Locate every Plasmodium parasite.
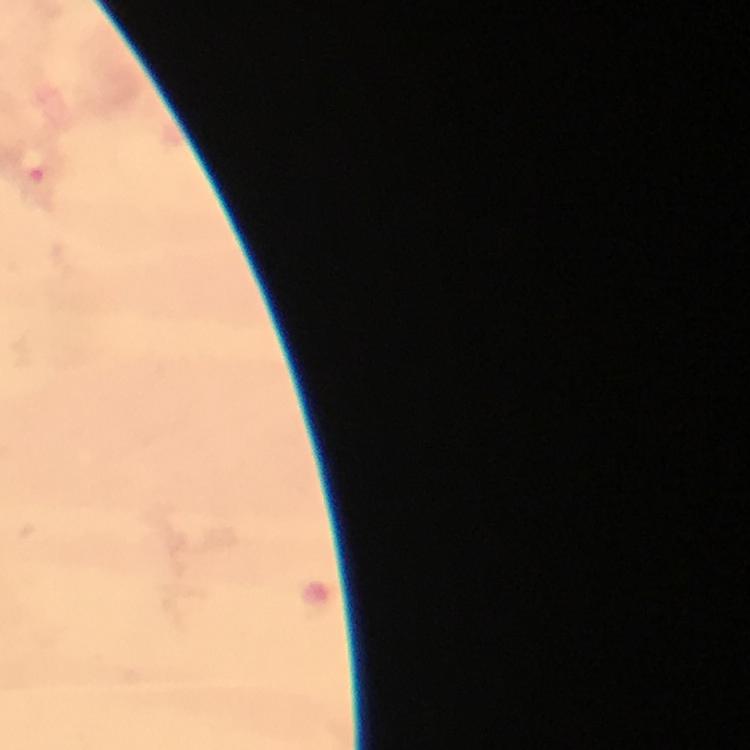

Approximate object centers, in pixels from the top-left corner.
Plasmodium parasites: (x=32, y=164).

Summary:
  - Preparation: thick smear
  - Stain: Giemsa
  - Capture: smartphone camera through the microscope
  - Context: from a malaria diagnostic workup
  - Image size: 750×750 pixels
  - Cropped from: a single field of view
  - Magnification: 100x
  - Immersion oil: applied